Locate and identify every blood parasite.
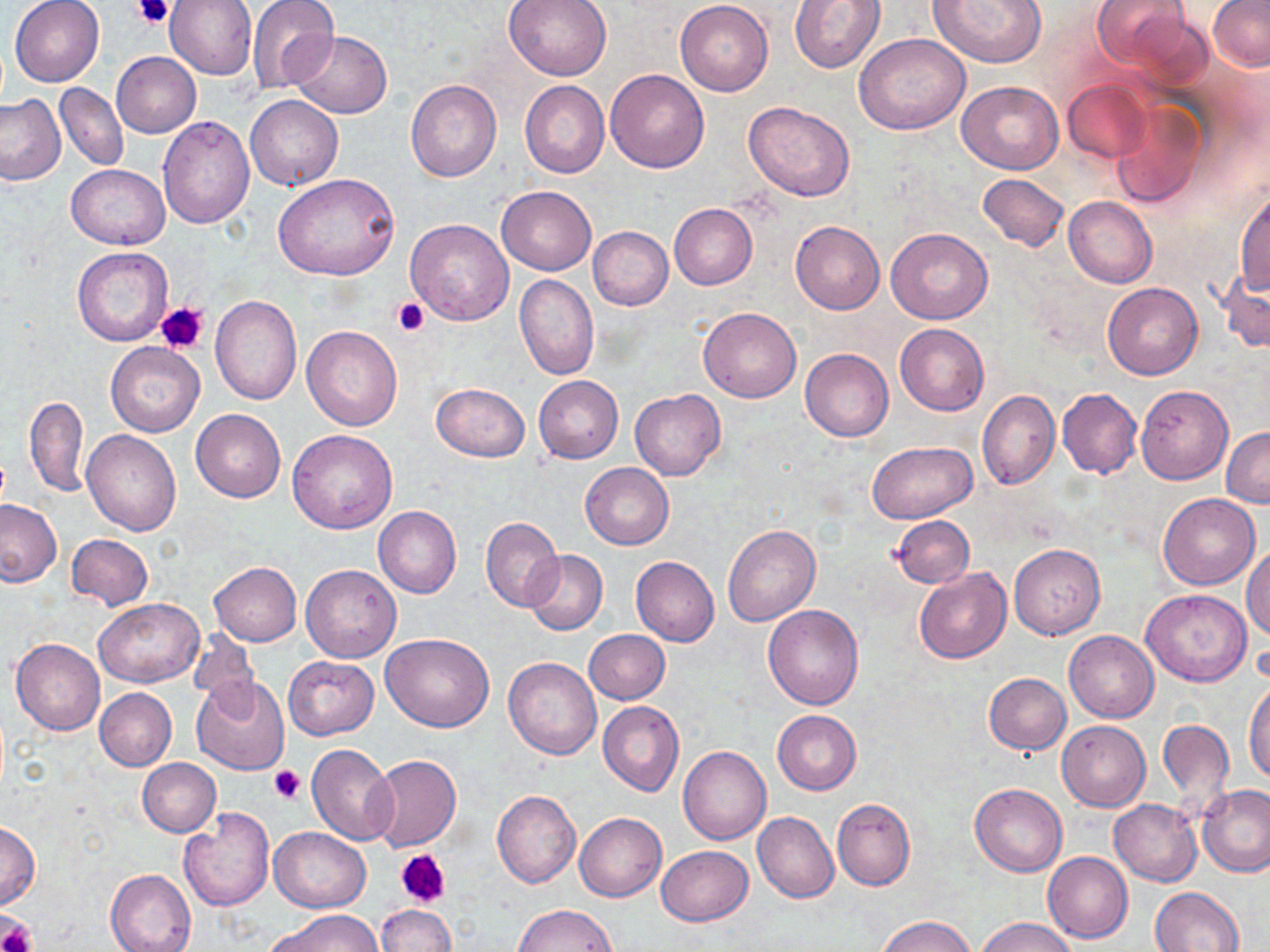
No blood parasites observed.

slide-level diagnosis = negative for blood parasites
uninfected red blood cell locations = approximate bounding boxes as named x1/y1/x2/y2 corners in pixels: (x1=9, y1=0, x2=105, y2=87), (x1=165, y1=0, x2=257, y2=80), (x1=504, y1=0, x2=613, y2=80), (x1=675, y1=0, x2=774, y2=96), (x1=788, y1=0, x2=885, y2=73), (x1=927, y1=0, x2=1048, y2=68), (x1=1090, y1=0, x2=1196, y2=79), (x1=247, y1=1, x2=339, y2=93), (x1=1208, y1=1, x2=1270, y2=71), (x1=291, y1=31, x2=391, y2=119), (x1=854, y1=33, x2=971, y2=135), (x1=111, y1=52, x2=201, y2=137), (x1=605, y1=69, x2=709, y2=173), (x1=1062, y1=79, x2=1153, y2=163), (x1=406, y1=80, x2=502, y2=182), (x1=520, y1=81, x2=610, y2=179), (x1=956, y1=81, x2=1064, y2=174), (x1=56, y1=83, x2=128, y2=172), (x1=0, y1=94, x2=65, y2=185), (x1=244, y1=95, x2=342, y2=191), (x1=1109, y1=98, x2=1208, y2=210), (x1=743, y1=102, x2=856, y2=201), (x1=158, y1=116, x2=254, y2=228), (x1=66, y1=164, x2=169, y2=249), (x1=274, y1=172, x2=401, y2=282), (x1=977, y1=173, x2=1069, y2=251), (x1=496, y1=185, x2=596, y2=276), (x1=1234, y1=187, x2=1269, y2=296), (x1=1063, y1=197, x2=1157, y2=288), (x1=669, y1=204, x2=757, y2=290), (x1=405, y1=218, x2=514, y2=325), (x1=791, y1=221, x2=884, y2=315), (x1=588, y1=226, x2=673, y2=309), (x1=886, y1=228, x2=993, y2=324), (x1=72, y1=246, x2=173, y2=347), (x1=1217, y1=267, x2=1270, y2=354), (x1=514, y1=273, x2=599, y2=380), (x1=1102, y1=281, x2=1202, y2=379), (x1=210, y1=294, x2=302, y2=405), (x1=698, y1=307, x2=802, y2=403), (x1=895, y1=324, x2=988, y2=416), (x1=302, y1=325, x2=403, y2=431), (x1=105, y1=342, x2=204, y2=437), (x1=799, y1=348, x2=893, y2=442), (x1=533, y1=375, x2=624, y2=463), (x1=430, y1=381, x2=530, y2=462), (x1=1135, y1=384, x2=1233, y2=483), (x1=1057, y1=387, x2=1142, y2=478), (x1=630, y1=388, x2=726, y2=479), (x1=977, y1=391, x2=1060, y2=489), (x1=25, y1=396, x2=89, y2=497), (x1=191, y1=408, x2=286, y2=503), (x1=1221, y1=428, x2=1270, y2=508), (x1=82, y1=429, x2=181, y2=535), (x1=287, y1=429, x2=398, y2=534), (x1=867, y1=440, x2=979, y2=523), (x1=579, y1=463, x2=674, y2=549), (x1=1158, y1=494, x2=1260, y2=590), (x1=0, y1=499, x2=62, y2=587), (x1=373, y1=505, x2=461, y2=598), (x1=480, y1=516, x2=563, y2=610), (x1=889, y1=516, x2=975, y2=587), (x1=723, y1=525, x2=820, y2=626), (x1=66, y1=533, x2=154, y2=610), (x1=1243, y1=542, x2=1270, y2=641), (x1=1009, y1=544, x2=1104, y2=638), (x1=522, y1=550, x2=608, y2=635), (x1=630, y1=556, x2=719, y2=646), (x1=209, y1=561, x2=302, y2=646), (x1=301, y1=564, x2=401, y2=663), (x1=914, y1=567, x2=1012, y2=663), (x1=1141, y1=589, x2=1252, y2=687), (x1=93, y1=597, x2=203, y2=687), (x1=763, y1=604, x2=864, y2=709), (x1=186, y1=628, x2=256, y2=701), (x1=583, y1=629, x2=670, y2=703), (x1=1065, y1=630, x2=1157, y2=723), (x1=380, y1=632, x2=494, y2=732), (x1=11, y1=638, x2=106, y2=735), (x1=284, y1=656, x2=378, y2=738), (x1=503, y1=657, x2=601, y2=759), (x1=984, y1=672, x2=1071, y2=754), (x1=1244, y1=675, x2=1270, y2=785), (x1=192, y1=676, x2=290, y2=775), (x1=94, y1=687, x2=177, y2=771), (x1=598, y1=702, x2=683, y2=796), (x1=772, y1=709, x2=861, y2=794), (x1=1157, y1=717, x2=1234, y2=812), (x1=1057, y1=721, x2=1150, y2=811), (x1=306, y1=744, x2=398, y2=846), (x1=678, y1=746, x2=771, y2=846), (x1=368, y1=755, x2=461, y2=853), (x1=138, y1=758, x2=220, y2=836), (x1=970, y1=782, x2=1067, y2=876), (x1=1197, y1=783, x2=1270, y2=878), (x1=493, y1=790, x2=581, y2=888), (x1=832, y1=798, x2=915, y2=891), (x1=1109, y1=799, x2=1202, y2=886), (x1=179, y1=807, x2=274, y2=911), (x1=574, y1=812, x2=666, y2=901), (x1=752, y1=812, x2=839, y2=903), (x1=0, y1=822, x2=39, y2=908), (x1=271, y1=826, x2=371, y2=912), (x1=656, y1=845, x2=753, y2=925), (x1=1042, y1=851, x2=1132, y2=942), (x1=105, y1=867, x2=196, y2=952), (x1=1150, y1=887, x2=1244, y2=951), (x1=375, y1=903, x2=456, y2=952), (x1=513, y1=904, x2=617, y2=951), (x1=266, y1=910, x2=382, y2=952), (x1=876, y1=914, x2=978, y2=952), (x1=974, y1=917, x2=1077, y2=952)
stain = May-Grünwald-Giemsa
magnification = 1000x
field of view = single
preparation = thin blood smear
image size = 1270×952 pixels
platelet locations = approximate bounding boxes as named x1/y1/x2/y2 corners in pixels: (x1=133, y1=0, x2=175, y2=28), (x1=392, y1=295, x2=428, y2=335), (x1=154, y1=300, x2=210, y2=354), (x1=270, y1=765, x2=306, y2=805), (x1=396, y1=848, x2=450, y2=908), (x1=0, y1=915, x2=36, y2=952)
modality = optical microscopy